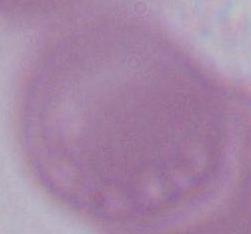
Summary:
  - Modality: micrograph
  - Identification: erythrocyte
  - Magnification: 1000x